Classify this cell by malaria status.
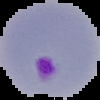

It is parasitized.

preparation: thin blood film
image_type: segmented cell region with the area outside set to black
image_size: 100×100 pixels